Describe the morphology of the red blood cells.
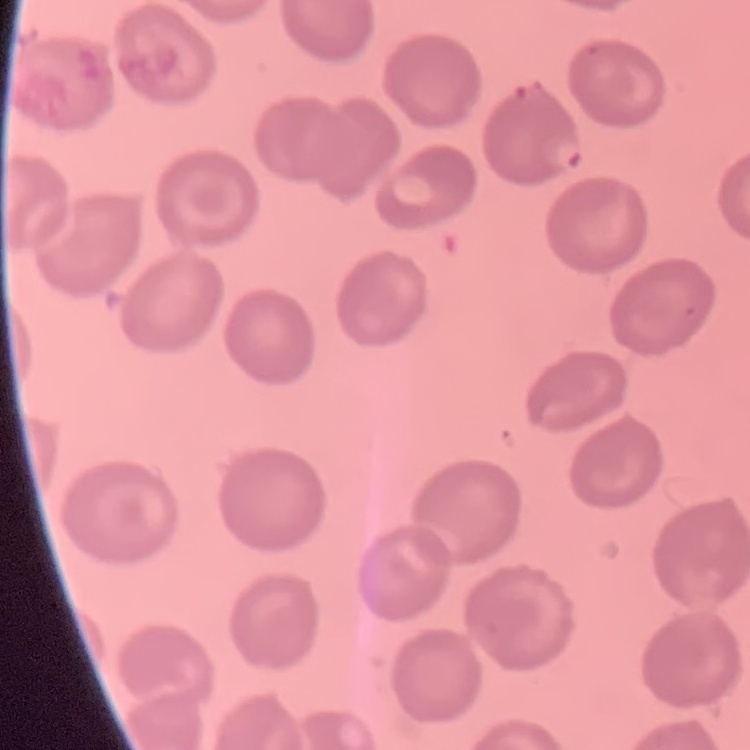
No rouleaux formation.

image type = one tile cut from a larger photomicrograph
preparation = thin blood film
stain = Field's or Giemsa